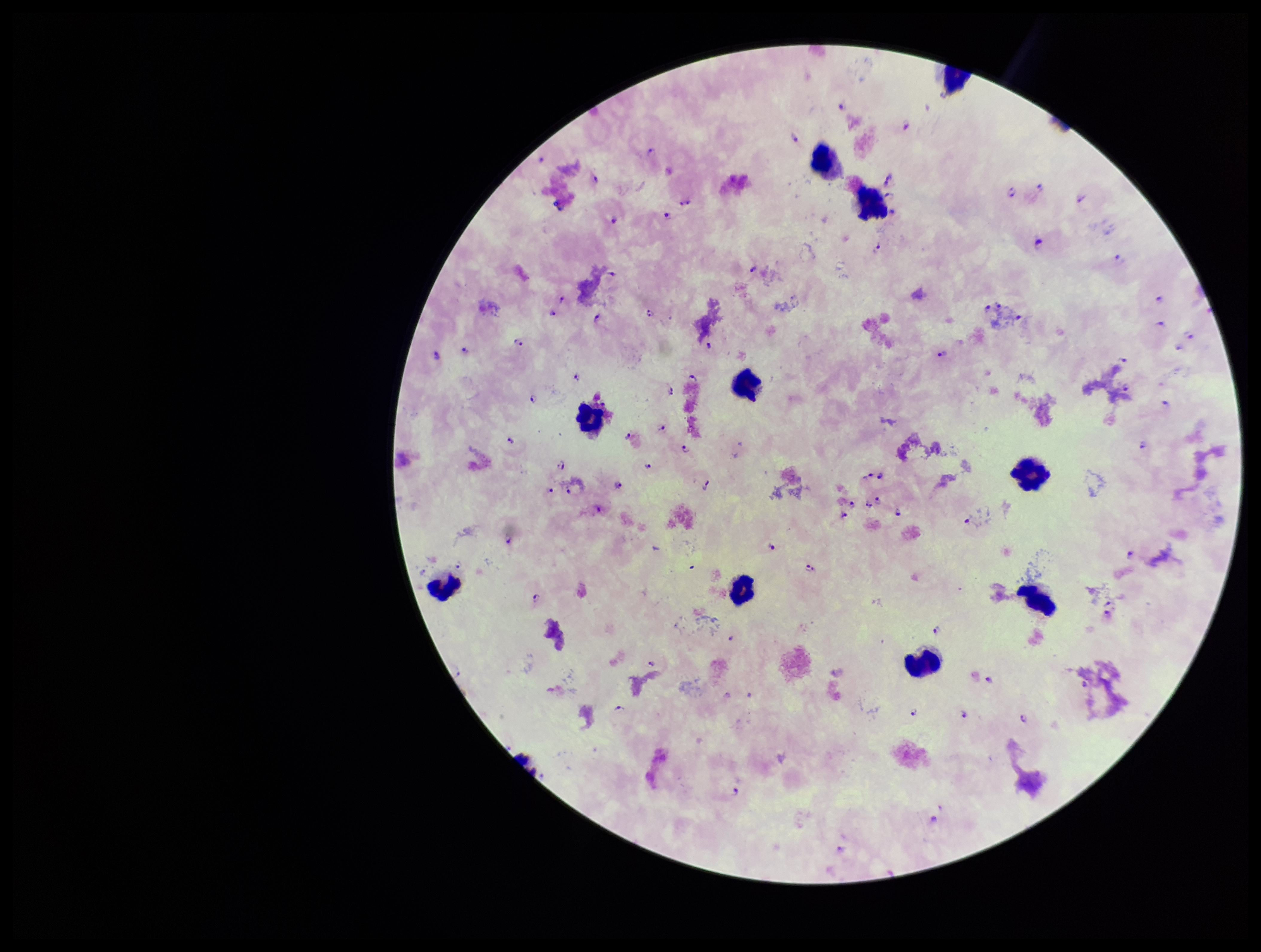
{
  "preparation": "thick smear",
  "parasite_count": 99,
  "patient_malaria_status": "positive",
  "capture": "smartphone photograph through the microscope eyepiece",
  "stain": "Giemsa",
  "leukocyte_count": 10,
  "species_reported_for_this_patient": "Plasmodium falciparum",
  "image_size": "1261×952 pixels",
  "plasmodium_parasites": "identified",
  "field_of_view": "one from this slide"
}